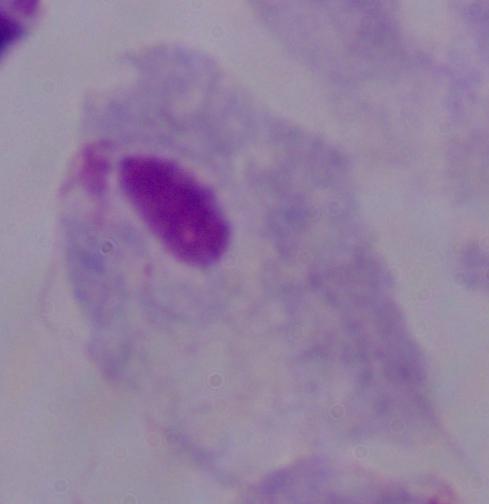

Summary:
  - Identification: trichomonad
  - Magnification: 1000x
  - Modality: photomicrograph